Give the position of every Plasmodium parasite visible.
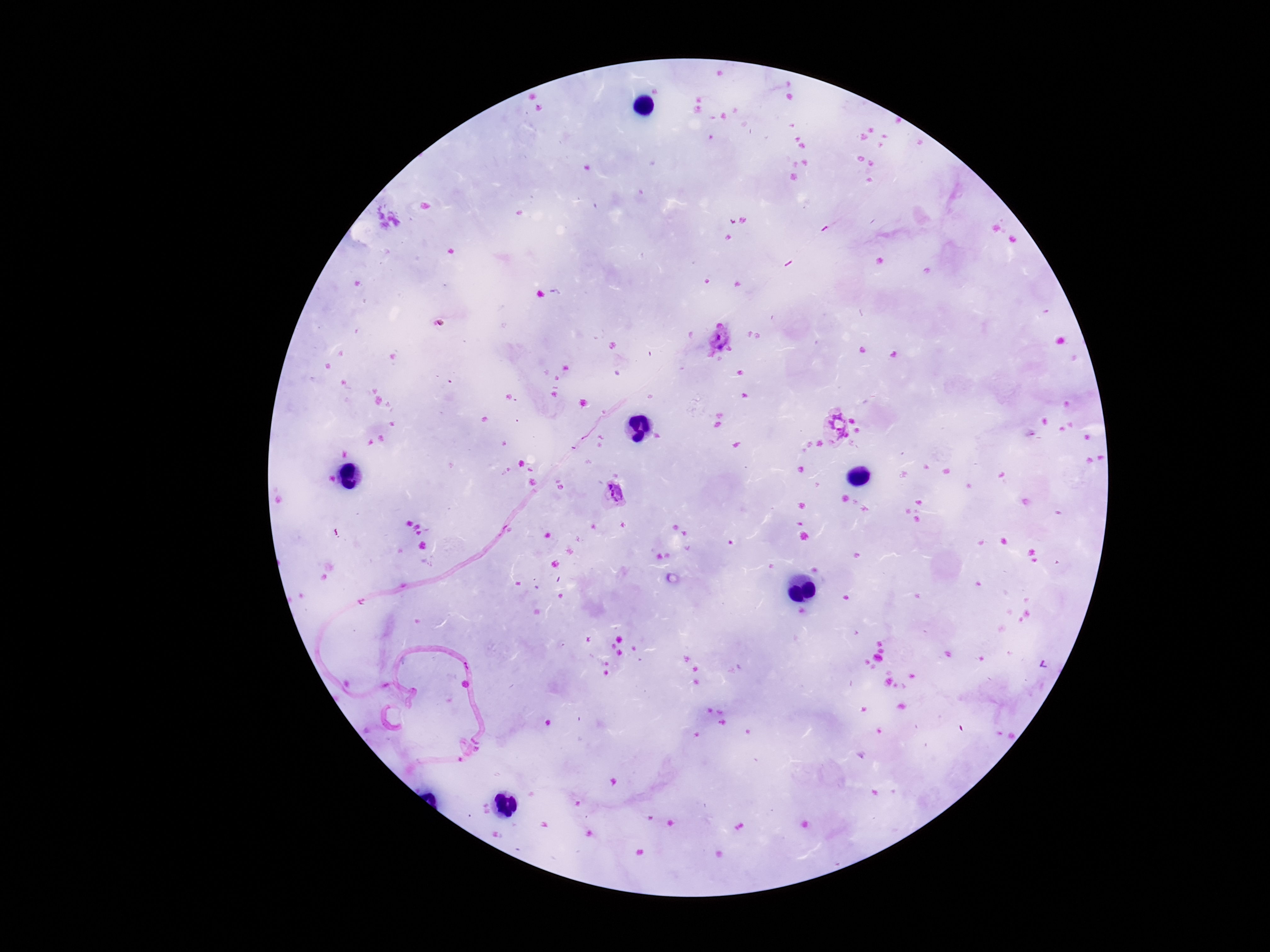

Approximate centers as {x, y} in pixels.
Plasmodium parasites: {718, 337}, {834, 427}, {612, 493}.

Summary:
  - Stain: Giemsa
  - Preparation: thick blood smear
  - Patient malaria status: infected
  - Image size: 1270×952 pixels
  - Field of view: single
  - Capture: smartphone camera through the microscope eyepiece
  - Magnification: 100x